Outline platelets.
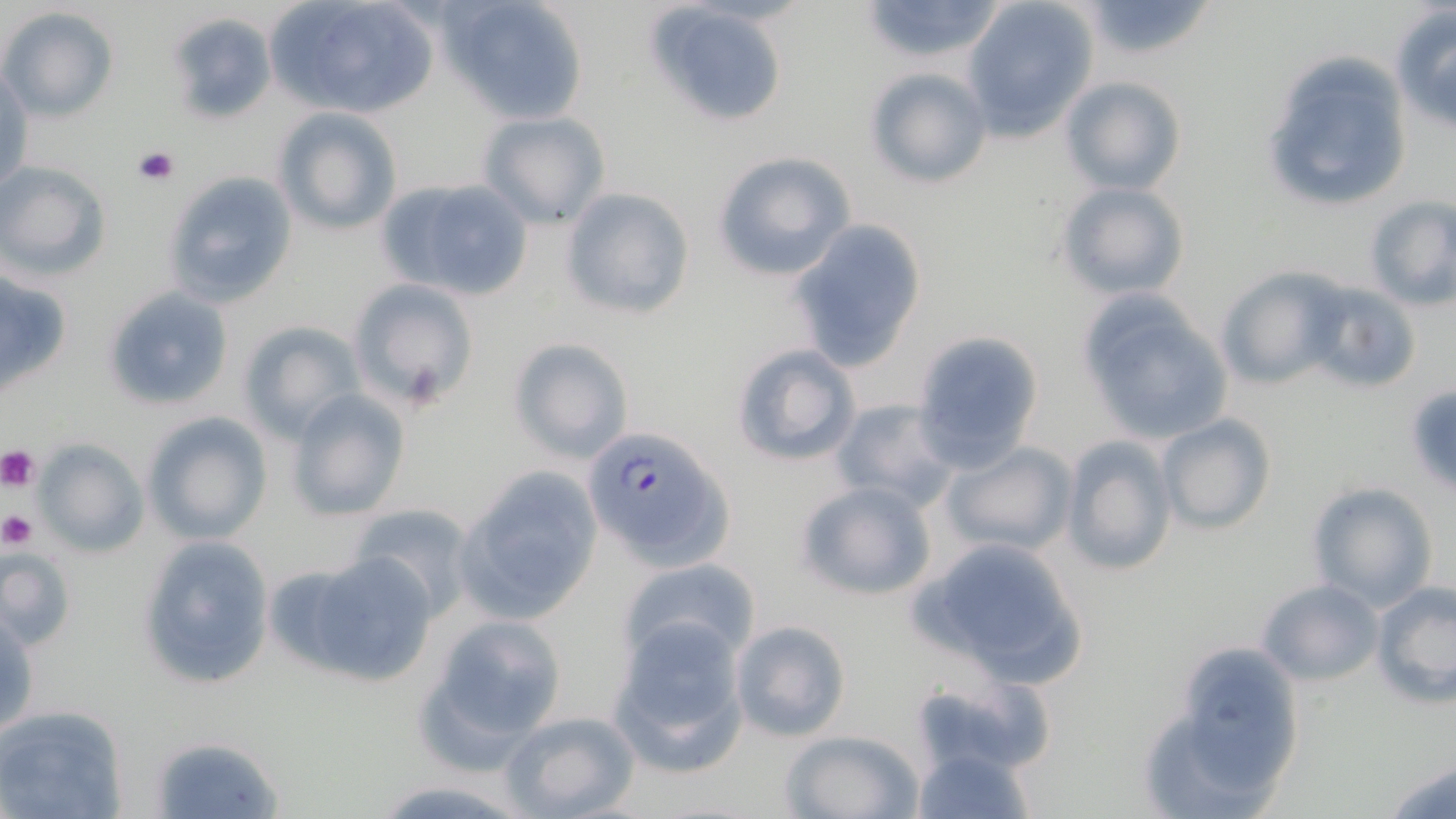

Approximate bounding boxes as (x1, y1, x2, y2) in pixels.
Platelets: (133, 146, 179, 185), (0, 446, 42, 493), (0, 512, 37, 549).

Summary:
  - Uninfected red blood cell locations: (268, 0, 441, 118), (442, 0, 593, 125), (857, 0, 1010, 64), (1080, 0, 1215, 61), (647, 1, 791, 126), (962, 1, 1098, 135), (1390, 6, 1456, 134), (0, 8, 119, 123), (165, 12, 277, 123), (1260, 46, 1411, 214), (865, 66, 990, 188), (2, 71, 32, 190), (1059, 77, 1186, 196), (276, 107, 401, 233), (477, 110, 611, 229), (712, 151, 855, 282), (0, 162, 112, 280), (163, 170, 298, 308), (375, 177, 536, 303), (1055, 181, 1189, 300), (559, 187, 697, 320), (1363, 195, 1456, 309), (790, 218, 927, 370), (1215, 266, 1347, 388), (0, 270, 72, 391), (348, 278, 481, 413), (1303, 280, 1423, 394), (104, 288, 232, 411), (1080, 298, 1232, 445), (238, 321, 364, 443), (912, 329, 1044, 469), (508, 338, 633, 464), (730, 342, 862, 467), (285, 390, 411, 522), (830, 397, 958, 509), (142, 412, 272, 545), (1156, 414, 1277, 534), (1060, 437, 1178, 576), (35, 438, 147, 558), (941, 443, 1074, 558), (454, 467, 603, 625), (795, 481, 936, 602), (1307, 483, 1436, 610), (348, 502, 480, 620), (138, 534, 274, 692), (915, 536, 1092, 688), (0, 546, 77, 652), (300, 552, 442, 687), (619, 556, 762, 667), (1258, 578, 1382, 685), (1372, 582, 1455, 707), (1, 611, 39, 738), (420, 613, 568, 761), (729, 619, 850, 742), (609, 620, 750, 768), (1148, 651, 1305, 813), (911, 677, 1053, 779), (0, 704, 128, 819), (500, 710, 640, 819), (781, 728, 924, 819), (149, 734, 285, 818), (911, 742, 1034, 818), (1385, 757, 1456, 817), (370, 778, 530, 817)
  - Plasmodium falciparum-infected red blood cell locations: (583, 424, 734, 566)
  - Slide-level diagnosis: Plasmodium falciparum
  - Magnification: 1000x
  - Stain: May-Grünwald-Giemsa
  - Field of view: single
  - Image size: 1456×819 pixels
  - Preparation: thin blood smear
  - Modality: light microscopy